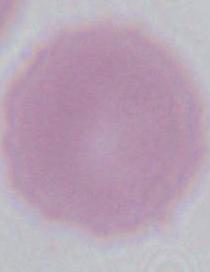

identification = erythrocyte
magnification = 1000x
modality = photomicrograph